Report the malaria status of this cell.
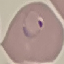
It is parasitized.

Cell patch, automatically extracted from a larger field of view and resized to 64 × 64 pixels. Acquired by smartphone through the microscope eyepiece. Giemsa stain. Thin blood film.